Locate and identify every blood parasite.
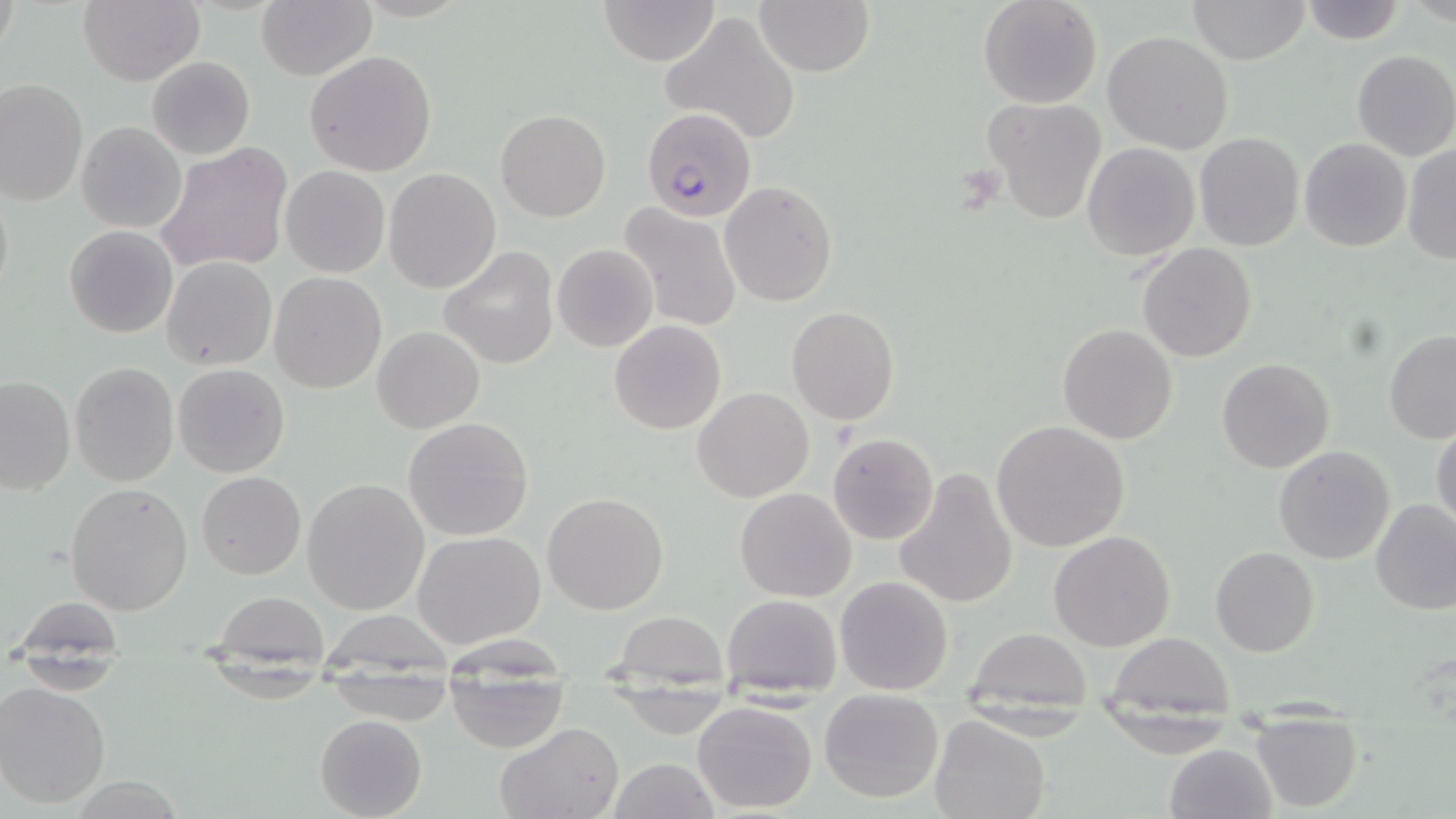
Approximate bounding boxes as (x1, y1, x2, y2) in pixels.
Plasmodium falciparum-infected red blood cells: (641, 108, 755, 221).
No Plasmodium ovale, Plasmodium malariae, Plasmodium vivax, Babesia divergens, or Trypanosoma brucei observed.

Summary:
  - Uninfected red blood cell locations: (78, 0, 203, 86), (599, 0, 720, 65), (978, 0, 1102, 109), (1185, 0, 1311, 65), (258, 1, 372, 80), (755, 1, 873, 77), (1298, 1, 1404, 46), (662, 11, 800, 143), (1103, 31, 1234, 155), (305, 49, 437, 177), (1351, 49, 1456, 160), (147, 56, 256, 159), (1, 78, 86, 207), (0, 94, 164, 217), (981, 97, 1107, 224), (495, 109, 611, 221), (78, 121, 186, 233), (1193, 132, 1305, 252), (1299, 138, 1413, 253), (156, 142, 294, 275), (1082, 142, 1200, 260), (1403, 144, 1455, 265), (280, 166, 389, 278), (384, 168, 501, 295), (719, 182, 838, 306), (619, 203, 743, 331), (63, 225, 178, 338), (552, 243, 658, 352), (1137, 244, 1256, 363), (440, 247, 560, 368), (163, 257, 277, 371), (267, 272, 387, 394), (786, 306, 899, 426), (610, 320, 725, 435), (1057, 323, 1178, 444), (372, 326, 484, 433), (1383, 328, 1456, 443), (1217, 357, 1334, 474), (69, 362, 179, 485), (173, 363, 290, 477), (0, 373, 75, 494), (694, 387, 814, 502), (404, 416, 533, 540), (992, 420, 1131, 552), (1432, 421, 1456, 533), (828, 434, 939, 545), (1274, 446, 1395, 565), (894, 467, 1018, 609), (197, 470, 305, 580), (302, 478, 431, 614), (65, 481, 195, 615), (734, 487, 856, 602), (541, 492, 669, 614), (1370, 502, 1456, 616), (1048, 530, 1176, 651), (412, 531, 546, 648), (1210, 547, 1320, 655), (834, 575, 955, 695), (210, 591, 332, 658), (722, 594, 842, 698), (15, 597, 127, 658), (613, 611, 727, 682), (965, 628, 1092, 716), (1103, 631, 1237, 711), (445, 675, 569, 753), (1, 681, 114, 808), (819, 687, 945, 803), (693, 701, 818, 814), (314, 714, 428, 818), (929, 714, 1051, 819), (1250, 716, 1362, 812), (493, 723, 624, 819), (1163, 742, 1278, 819), (608, 758, 721, 819)
  - Slide-level diagnosis: Plasmodium falciparum
  - Modality: light microscopy
  - Stain: May-Grünwald-Giemsa
  - Field of view: single
  - Image size: 1456×819 pixels
  - Preparation: thin blood smear
  - Magnification: 1000x